Find each parasitized RBC.
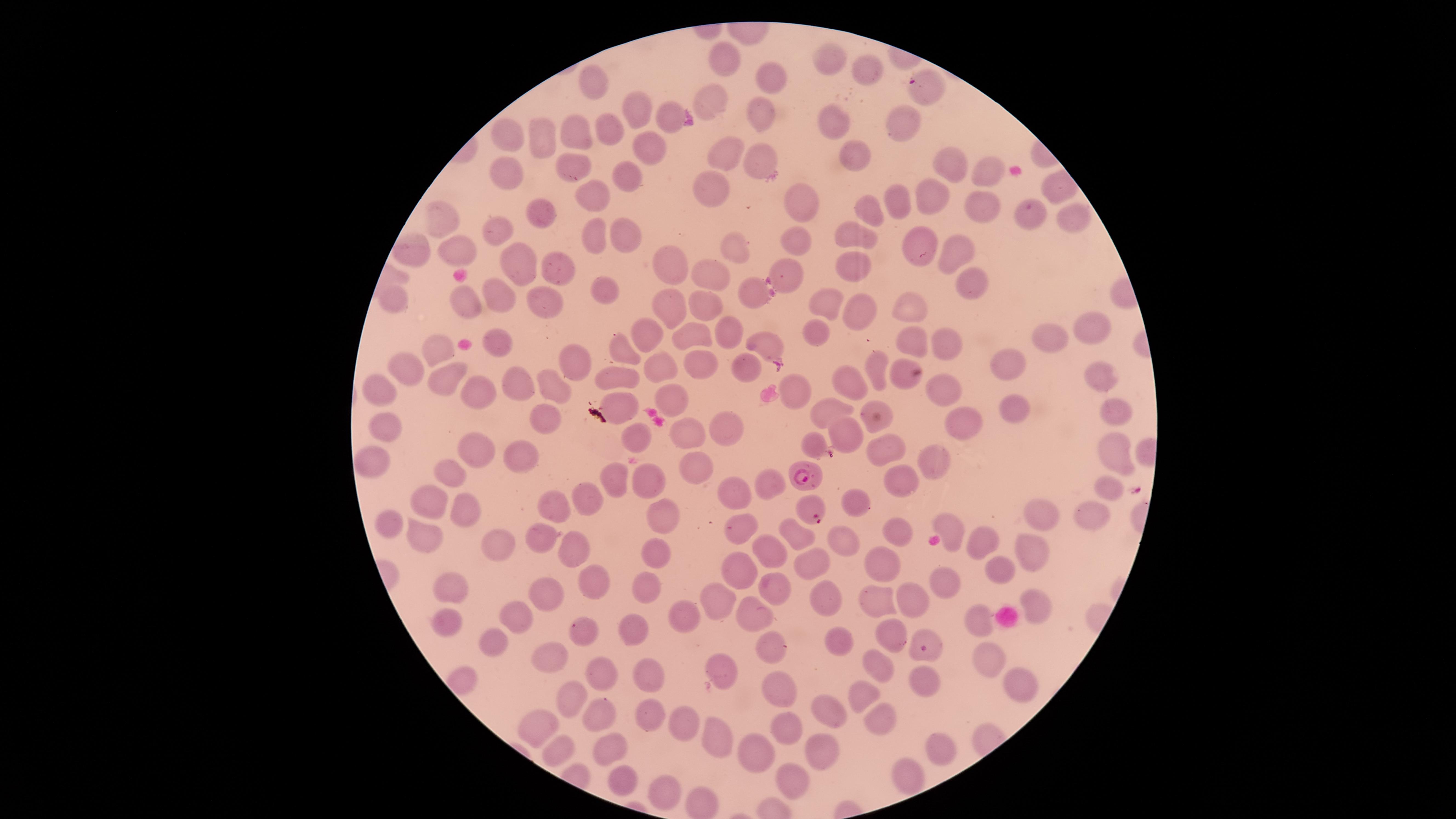
Approximate marker points as [x, y] in pixels.
Parasitized RBCs: [806, 475], [810, 509].

capture = smartphone photograph through the microscope eyepiece
image size = 1456×819 pixels
field of view = single
visible region = circular
stain = Giemsa
species = Plasmodium falciparum
uninfected RBCs = approximate marker points as [x, y] in pixels: [830, 62], [722, 63], [866, 67], [597, 82], [771, 82], [927, 94], [709, 98], [638, 111], [753, 115], [670, 118], [833, 118], [905, 126], [608, 128], [576, 131], [508, 136], [546, 139], [646, 147], [851, 151], [760, 158], [726, 160], [572, 163], [950, 164], [988, 168], [506, 177], [630, 178], [710, 186], [931, 191], [592, 192], [801, 193], [895, 197], [979, 202], [867, 210], [536, 211], [445, 218], [1030, 219], [1068, 219], [851, 228], [495, 229], [629, 234], [595, 235], [795, 243], [915, 244], [731, 250], [948, 252], [412, 253], [462, 256], [663, 262], [520, 264], [850, 265], [554, 267], [791, 271], [713, 276], [971, 283], [601, 289], [748, 291], [494, 295], [548, 299], [708, 300], [396, 302], [464, 303], [667, 305], [906, 305], [829, 307], [852, 311], [1087, 326], [721, 327], [691, 333], [815, 333], [1048, 333], [647, 336], [907, 337], [502, 339], [765, 342], [948, 342], [441, 348], [624, 348], [575, 360], [699, 361], [878, 364], [407, 367], [899, 367], [1005, 367], [740, 368], [656, 369], [1102, 376], [615, 378], [445, 380], [851, 381], [515, 383], [548, 386], [941, 387], [794, 389], [378, 391], [477, 394], [675, 396], [1014, 407], [827, 410], [871, 410], [1118, 410], [624, 411], [539, 418], [971, 419], [392, 424], [721, 424], [683, 430], [641, 437], [816, 439], [880, 448], [1115, 449], [483, 451], [517, 451], [934, 462], [368, 465], [697, 468], [451, 471], [612, 474], [894, 480], [645, 483], [770, 485], [1104, 488], [585, 496], [730, 496], [435, 498], [551, 500], [856, 501], [467, 512], [1095, 512], [664, 514], [1045, 514], [388, 521], [943, 525], [734, 528], [900, 532], [541, 533], [976, 535], [797, 538], [433, 541], [495, 541], [841, 541], [577, 547], [768, 547], [1032, 549], [655, 552], [813, 561], [880, 562], [991, 565], [737, 571], [597, 579], [454, 581], [941, 582], [651, 587], [772, 587], [550, 596], [882, 598], [1036, 599], [720, 601], [827, 601], [910, 602], [749, 611], [980, 615], [684, 616], [520, 617], [445, 619], [583, 630], [642, 631], [887, 634], [835, 638], [492, 640], [776, 646], [547, 654], [934, 655], [986, 656], [875, 661], [724, 664], [647, 668], [605, 674], [928, 682], [777, 685], [1027, 690], [864, 695], [570, 696], [830, 710], [609, 713], [652, 713], [877, 721], [784, 722], [540, 725], [682, 725], [718, 736], [610, 739], [819, 749], [941, 750], [554, 751], [757, 757], [619, 776], [907, 777], [790, 781], [669, 787]
preparation = thin blood smear